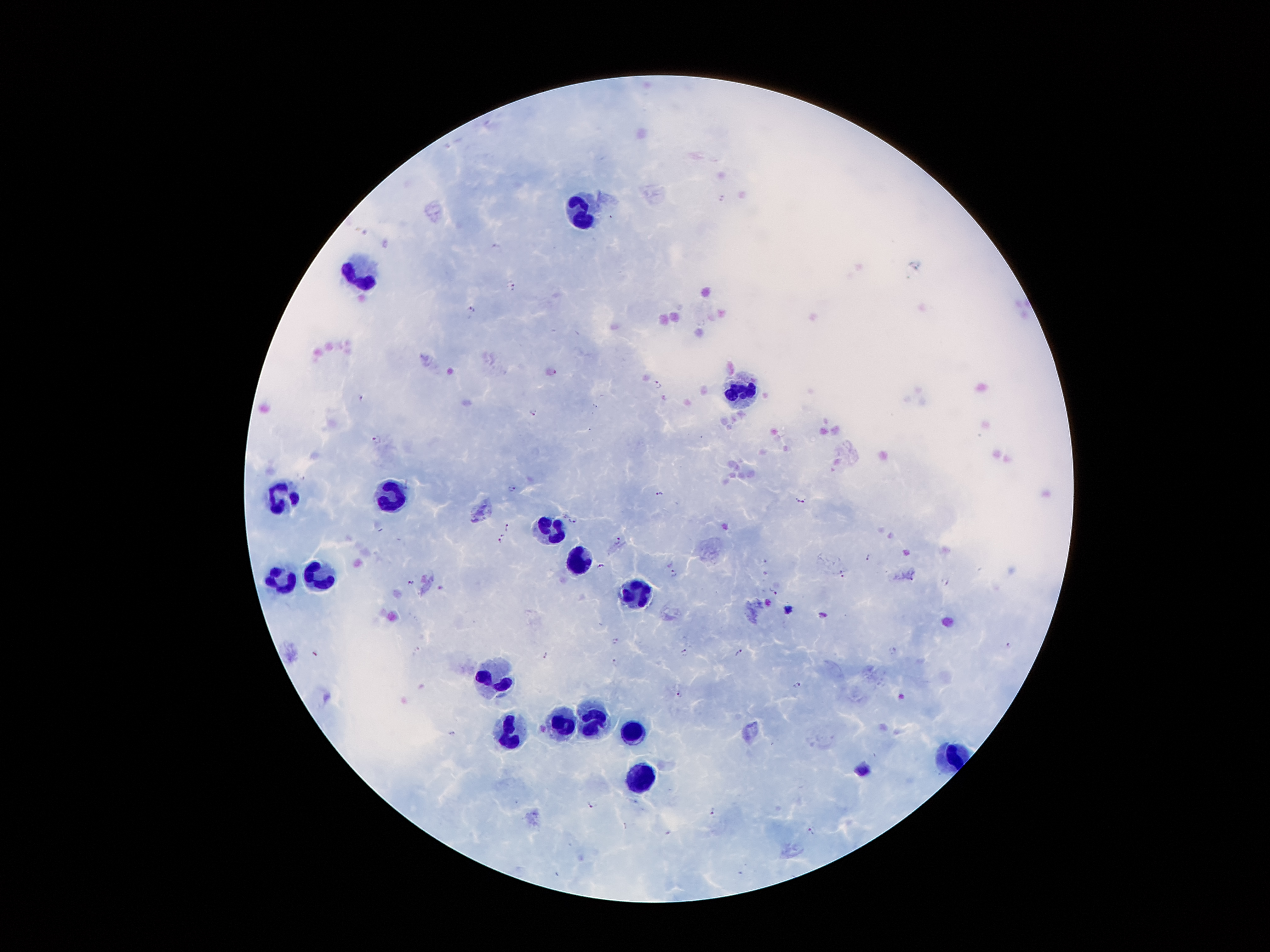
Approximate object centers, in pixels from the top-left corner.
Summary:
  - Leukocyte locations: (x=585, y=212), (x=359, y=270), (x=740, y=392), (x=391, y=496), (x=281, y=498), (x=550, y=529), (x=578, y=561), (x=320, y=574), (x=283, y=582), (x=633, y=591), (x=493, y=679), (x=592, y=718), (x=565, y=725), (x=509, y=733), (x=636, y=735), (x=948, y=753), (x=643, y=775)
  - Plasmodium parasite locations: (x=496, y=246), (x=512, y=286), (x=471, y=309), (x=551, y=371), (x=657, y=382), (x=362, y=396), (x=533, y=412), (x=376, y=439), (x=512, y=487), (x=659, y=493), (x=801, y=499), (x=573, y=518), (x=507, y=526), (x=499, y=539), (x=617, y=540), (x=870, y=557), (x=600, y=566), (x=673, y=572), (x=842, y=572), (x=945, y=581), (x=411, y=583), (x=772, y=590), (x=615, y=640), (x=1010, y=645), (x=893, y=650), (x=417, y=651), (x=684, y=652), (x=739, y=652), (x=315, y=654), (x=545, y=654), (x=614, y=662), (x=796, y=684), (x=681, y=694), (x=451, y=732), (x=591, y=804), (x=712, y=812), (x=811, y=831)
  - Stain: Giemsa
  - Capture: smartphone through the microscope eyepiece
  - Patient malaria status: infected with Plasmodium falciparum
  - Preparation: thick blood smear
  - Magnification: 100x
  - Image size: 1270×952 pixels
  - Field of view: one from this slide